State the blood parasite species.
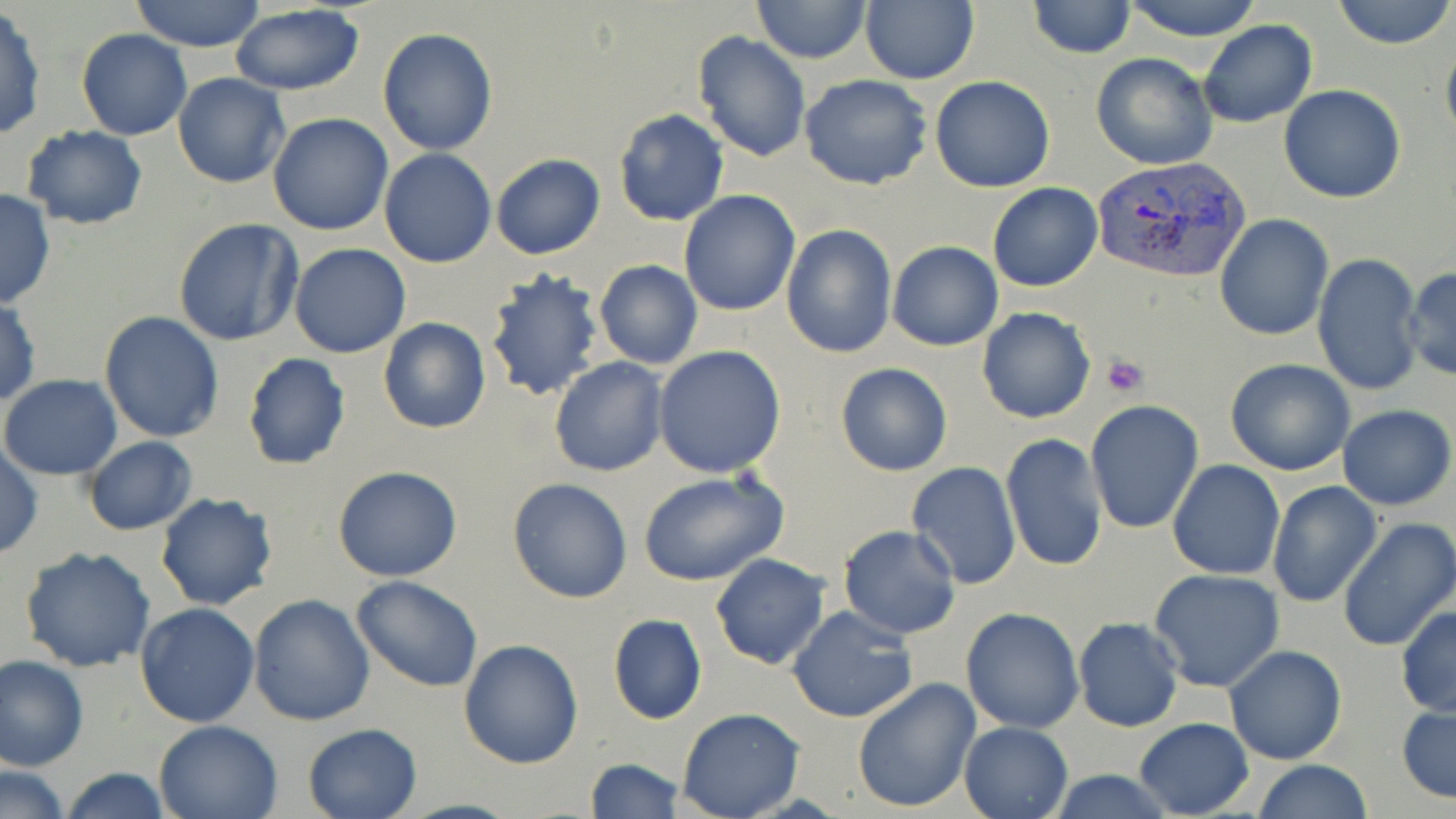
Plasmodium vivax.

Approximate bounding boxes as named x1/y1/x2/y2 corners in pixels. Plasmodium vivax-infected red blood cell locations: (x1=1092, y1=154, x2=1251, y2=283). Uninfected red blood cell locations: (x1=130, y1=0, x2=267, y2=52), (x1=750, y1=0, x2=871, y2=65), (x1=861, y1=0, x2=979, y2=84), (x1=1120, y1=0, x2=1263, y2=41), (x1=1332, y1=0, x2=1455, y2=50), (x1=1027, y1=1, x2=1137, y2=59), (x1=228, y1=5, x2=366, y2=95), (x1=0, y1=8, x2=46, y2=140), (x1=1198, y1=21, x2=1318, y2=129), (x1=377, y1=27, x2=498, y2=155), (x1=76, y1=29, x2=192, y2=142), (x1=694, y1=31, x2=811, y2=161), (x1=1441, y1=36, x2=1456, y2=154), (x1=1091, y1=53, x2=1217, y2=170), (x1=174, y1=72, x2=289, y2=188), (x1=799, y1=73, x2=932, y2=191), (x1=929, y1=76, x2=1055, y2=192), (x1=1279, y1=85, x2=1405, y2=203), (x1=611, y1=107, x2=731, y2=227), (x1=267, y1=112, x2=394, y2=235), (x1=21, y1=126, x2=149, y2=229), (x1=378, y1=148, x2=497, y2=268), (x1=492, y1=153, x2=605, y2=258), (x1=987, y1=183, x2=1102, y2=292), (x1=0, y1=188, x2=55, y2=310), (x1=678, y1=190, x2=800, y2=316), (x1=1214, y1=213, x2=1333, y2=341), (x1=173, y1=219, x2=304, y2=347), (x1=782, y1=223, x2=897, y2=359), (x1=886, y1=241, x2=1003, y2=351), (x1=289, y1=243, x2=411, y2=358), (x1=1314, y1=252, x2=1425, y2=399), (x1=594, y1=260, x2=704, y2=369), (x1=1403, y1=265, x2=1456, y2=381), (x1=482, y1=266, x2=606, y2=399), (x1=0, y1=297, x2=40, y2=408), (x1=977, y1=308, x2=1096, y2=424), (x1=99, y1=310, x2=224, y2=443), (x1=378, y1=317, x2=491, y2=434), (x1=654, y1=346, x2=786, y2=478), (x1=241, y1=352, x2=352, y2=470), (x1=550, y1=358, x2=668, y2=477), (x1=1224, y1=358, x2=1355, y2=475), (x1=835, y1=362, x2=954, y2=477), (x1=0, y1=374, x2=123, y2=479), (x1=1086, y1=400, x2=1205, y2=534), (x1=1337, y1=403, x2=1455, y2=510), (x1=1000, y1=434, x2=1108, y2=573), (x1=82, y1=436, x2=198, y2=536), (x1=0, y1=441, x2=43, y2=561), (x1=1168, y1=459, x2=1286, y2=581), (x1=904, y1=461, x2=1021, y2=590), (x1=333, y1=464, x2=464, y2=582), (x1=636, y1=470, x2=788, y2=586), (x1=507, y1=479, x2=633, y2=603), (x1=1266, y1=481, x2=1382, y2=608), (x1=154, y1=492, x2=278, y2=611), (x1=1335, y1=517, x2=1456, y2=652), (x1=838, y1=525, x2=962, y2=640), (x1=19, y1=544, x2=156, y2=672), (x1=709, y1=553, x2=831, y2=671), (x1=1149, y1=568, x2=1285, y2=691), (x1=351, y1=575, x2=483, y2=692), (x1=249, y1=593, x2=377, y2=726), (x1=135, y1=602, x2=259, y2=727), (x1=1395, y1=604, x2=1456, y2=718), (x1=786, y1=605, x2=917, y2=723), (x1=960, y1=606, x2=1085, y2=732), (x1=607, y1=613, x2=707, y2=724), (x1=1073, y1=618, x2=1183, y2=733), (x1=458, y1=639, x2=584, y2=769), (x1=1224, y1=645, x2=1347, y2=766), (x1=0, y1=654, x2=88, y2=771), (x1=852, y1=677, x2=982, y2=814), (x1=1397, y1=701, x2=1456, y2=806), (x1=676, y1=709, x2=803, y2=819), (x1=1133, y1=717, x2=1253, y2=818), (x1=153, y1=719, x2=283, y2=819), (x1=958, y1=720, x2=1072, y2=819), (x1=301, y1=722, x2=422, y2=819), (x1=584, y1=757, x2=685, y2=819), (x1=1251, y1=760, x2=1373, y2=819), (x1=2, y1=764, x2=71, y2=818), (x1=58, y1=767, x2=174, y2=819), (x1=1044, y1=769, x2=1178, y2=818). Platelet locations: (x1=1102, y1=354, x2=1149, y2=396). Thin blood film. Single field of view. Image is 1456×819 pixels. Optical microscopy. 1000x magnification. May-Grünwald-Giemsa-stained preparation.